Report the malaria status of this cell.
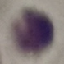

Uninfected.

Automatically extracted cell patch, resized to 64 × 64 pixels. Giemsa-stained preparation. Acquired by smartphone through the microscope eyepiece. Thin blood smear.